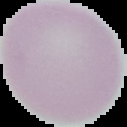 The area outside the segmented cell region is set to black. Malaria status: uninfected. Image is 127×127 pixels. From a thin blood smear.